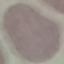
Summary:
  - Malaria status: uninfected
  - Stain: Giemsa
  - Image type: cell patch, automatically extracted from a larger field of view and resized to 64 × 64 pixels
  - Preparation: thin blood smear
  - Capture: smartphone camera at the microscope eyepiece